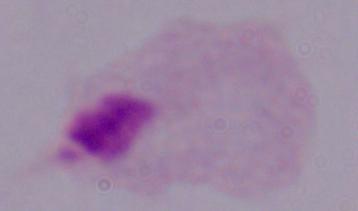

magnification = 1000x
modality = micrograph
identification = trichomonad